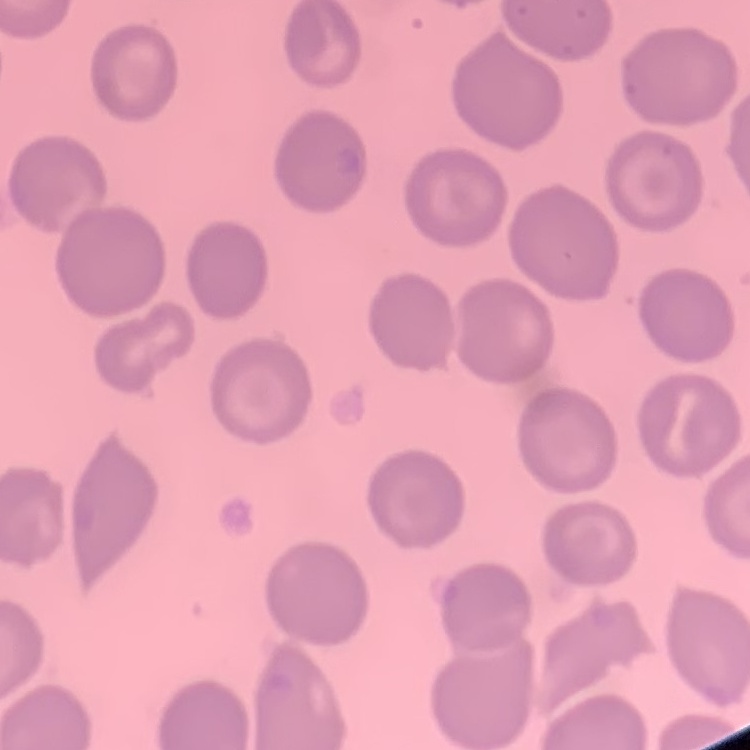

The erythrocytes show no rouleaux formation. Square crop of a larger photomicrograph. Stained with either Field's or Giemsa. Thin blood film.